Name the cell type shown.
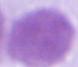

An erythrocyte.

modality: photomicrograph
magnification: 1000x